State which parasite is depicted.
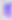
Toxoplasma gondii.

modality = photomicrograph
magnification = 400x